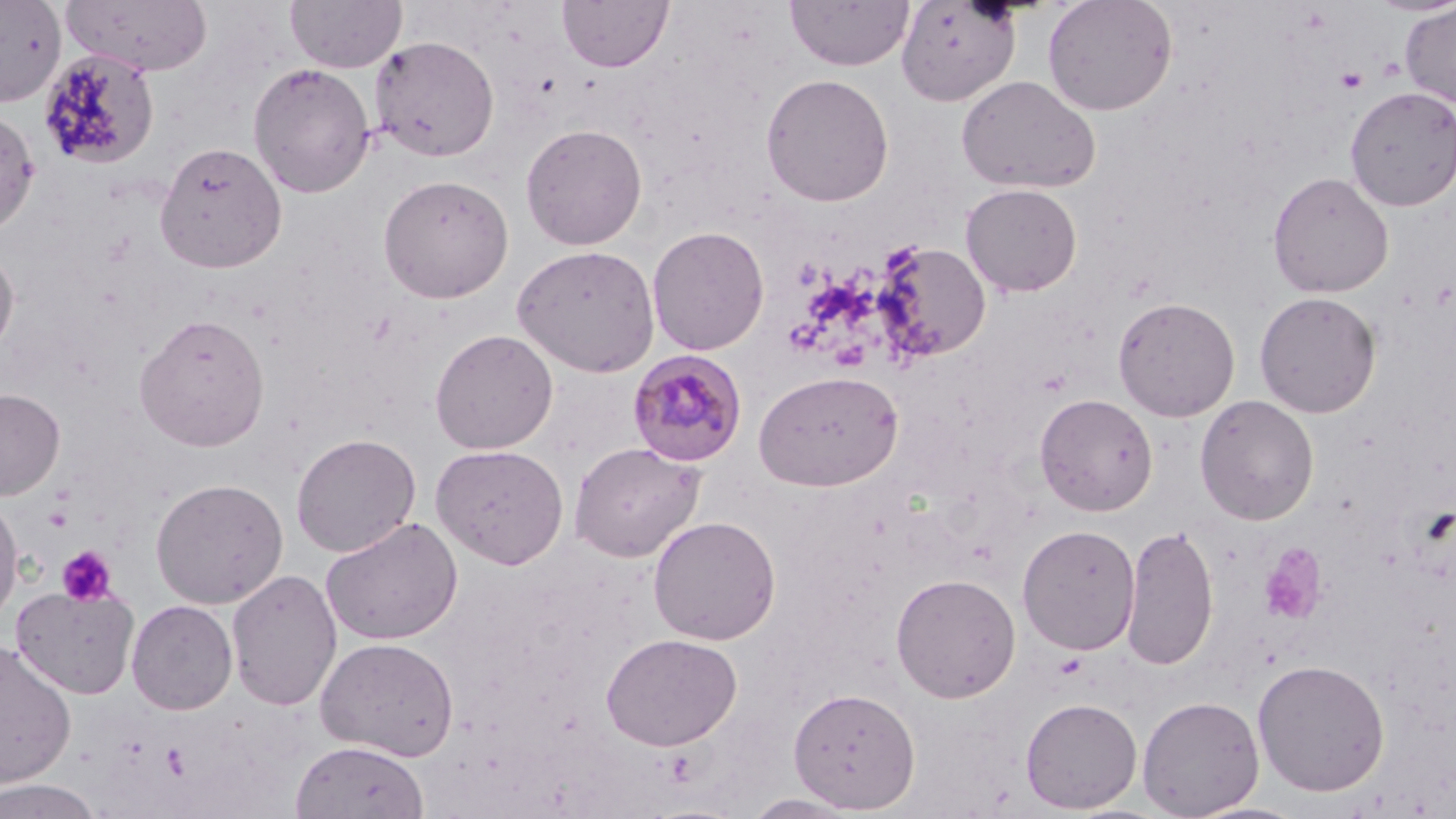
Approximate bounding boxes as (x1,y1)-(x2,y2) corner pairs in pixels. Uninfected red blood cell locations: (0,0)-(66,107), (63,0)-(214,76), (285,0)-(406,73), (557,0)-(673,73), (785,0)-(914,71), (1042,0)-(1178,116), (896,1)-(1022,107), (1399,3)-(1456,107), (369,36)-(500,162), (37,48)-(161,171), (247,62)-(376,198), (760,73)-(894,207), (956,74)-(1102,194), (1345,85)-(1456,212), (0,108)-(40,234), (520,123)-(648,250), (154,141)-(288,274), (1267,171)-(1394,298), (377,173)-(514,303), (960,183)-(1082,296), (647,225)-(769,356), (876,241)-(990,362), (512,244)-(661,377), (0,245)-(19,360), (1254,291)-(1381,418), (1113,296)-(1240,421), (133,313)-(270,451), (429,329)-(558,454), (754,369)-(904,492), (0,388)-(65,500), (1035,393)-(1158,516), (1194,395)-(1319,525), (291,433)-(421,557), (569,441)-(705,562), (430,443)-(569,569), (150,477)-(288,609), (0,492)-(24,626), (321,515)-(463,646), (647,515)-(781,645), (1017,524)-(1140,655), (1121,524)-(1219,671), (226,568)-(342,712), (890,572)-(1021,703), (10,583)-(140,699), (126,599)-(238,714), (601,632)-(743,750), (315,636)-(459,760), (0,638)-(77,788), (1252,658)-(1390,796), (788,686)-(920,812), (1137,695)-(1264,818), (1020,697)-(1142,813), (290,740)-(429,818), (0,778)-(103,819), (743,792)-(862,818). Plasmodium malariae-infected red blood cell locations: (626,349)-(748,467). Platelet locations: (1377,55)-(1404,82), (1336,67)-(1368,93), (793,259)-(824,289), (45,505)-(73,532), (1259,544)-(1328,625), (57,546)-(116,606), (160,742)-(191,780). Slide-level diagnosis: Plasmodium malariae. Image is 1456×819 pixels. Optical microscopy. 1000x magnification. May-Grünwald-Giemsa stain. Thin blood smear. Single field of view.